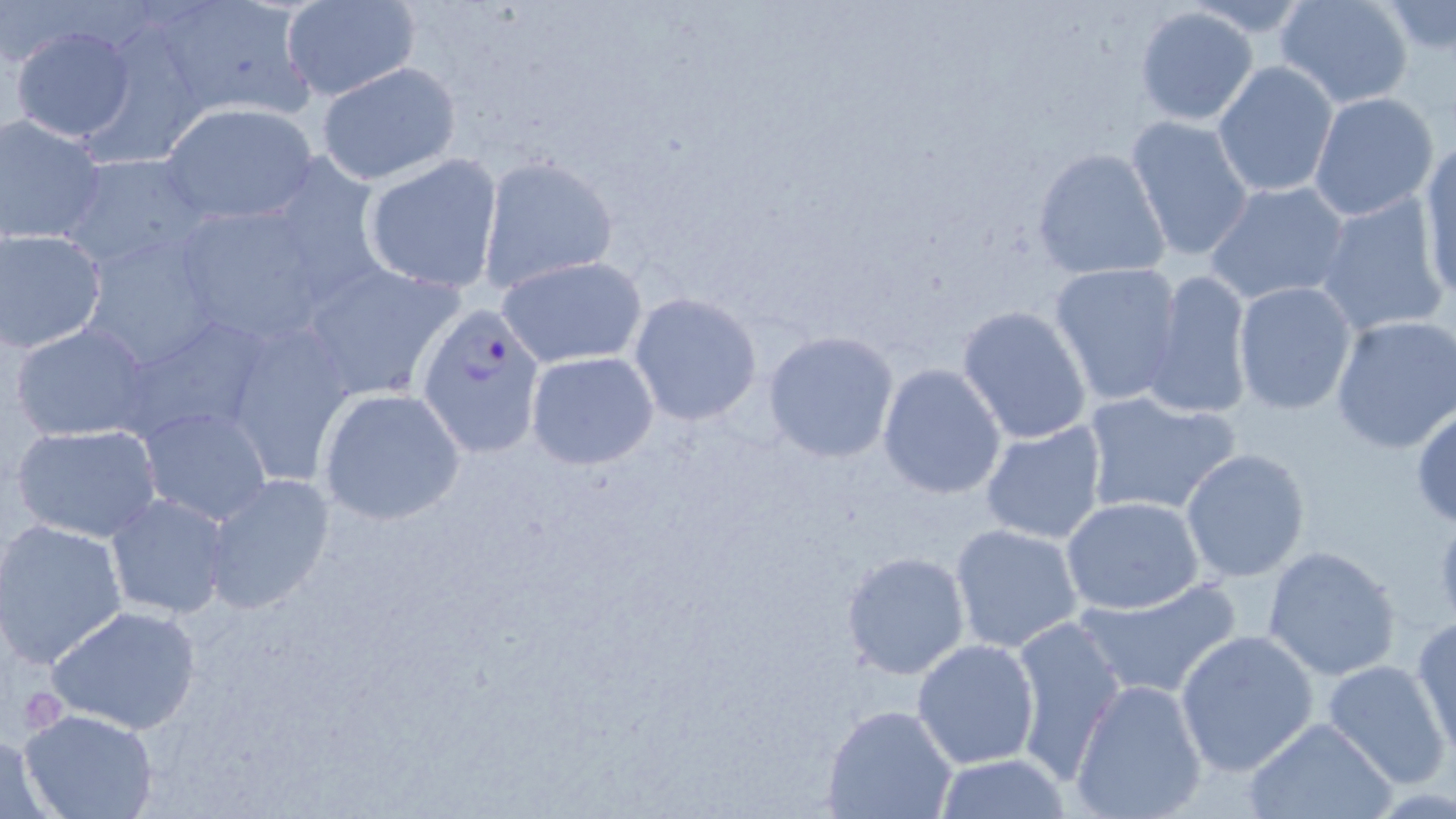

Summary:
  - Coordinate format: approximate bounding boxes as (x1,y1)-(x2,y2) corner pairs in pixels
  - Plasmodium falciparum-infected red blood cell locations: (416,303)-(546,457)
  - Uninfected red blood cell locations: (1274,0)-(1415,109), (281,2)-(420,101), (1379,2)-(1456,57), (153,4)-(318,123), (1132,6)-(1259,127), (8,25)-(138,144), (1212,61)-(1339,197), (316,63)-(462,186), (1309,92)-(1440,222), (160,103)-(318,226), (1,114)-(108,247), (1125,115)-(1255,263), (1417,143)-(1456,302), (1031,146)-(1170,281), (60,152)-(211,272), (361,154)-(504,293), (477,156)-(618,292), (1205,180)-(1351,306), (1315,192)-(1448,336), (170,200)-(335,345), (0,228)-(110,355), (79,230)-(229,375), (497,255)-(647,368), (296,260)-(467,403), (1049,262)-(1183,406), (1142,269)-(1255,420), (1234,282)-(1359,415), (629,292)-(763,426), (955,305)-(1094,446), (1331,315)-(1456,451), (218,317)-(357,483), (120,318)-(270,447), (8,322)-(156,443), (762,329)-(900,464), (524,349)-(660,469), (877,363)-(1007,500), (317,387)-(465,526), (1080,388)-(1242,518), (1410,403)-(1456,528), (138,405)-(273,527), (978,418)-(1109,544), (9,423)-(163,542), (1180,448)-(1312,581), (202,474)-(336,616), (106,492)-(231,620), (1061,495)-(1209,615), (1431,510)-(1456,627), (0,520)-(129,669), (948,522)-(1086,654), (1262,545)-(1402,681), (840,549)-(971,681), (1075,578)-(1241,699), (45,604)-(202,736), (1010,614)-(1125,781), (1410,615)-(1455,758), (1174,630)-(1321,776), (912,638)-(1040,771), (1322,659)-(1452,790), (1068,678)-(1209,819), (822,704)-(958,819), (19,709)-(161,819), (1242,715)-(1397,819), (0,730)-(56,817), (933,754)-(1071,818)
  - Slide-level diagnosis: Plasmodium falciparum
  - Preparation: thin blood film
  - Image size: 1456×819 pixels
  - Stain: May-Grünwald-Giemsa
  - Magnification: 1000x
  - Field of view: one of a larger specimen
  - Modality: light microscopy